State which cell type is depicted.
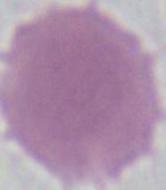

An erythrocyte.

modality = photomicrograph
magnification = 1000x